Name the parasite shown.
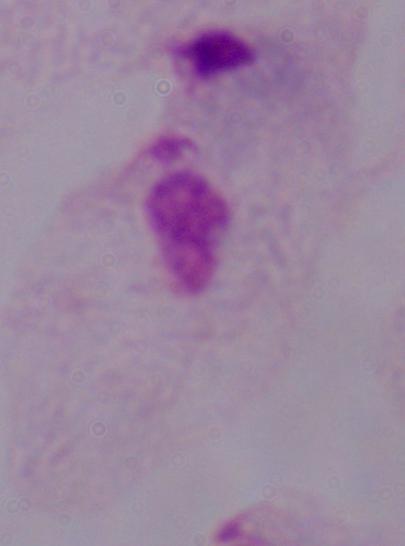
This is a trichomonad.

1000x magnification. Micrograph.